Name the cell type shown.
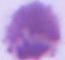

This is an erythrocyte.

Summary:
  - Magnification: 1000x
  - Modality: micrograph